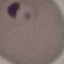
Result: malaria parasites identified. Thin smear of blood. Giemsa stain. Automatically extracted cell patch, resized to 64 × 64 pixels. Acquired by smartphone through the microscope eyepiece.